Name the blood parasite species.
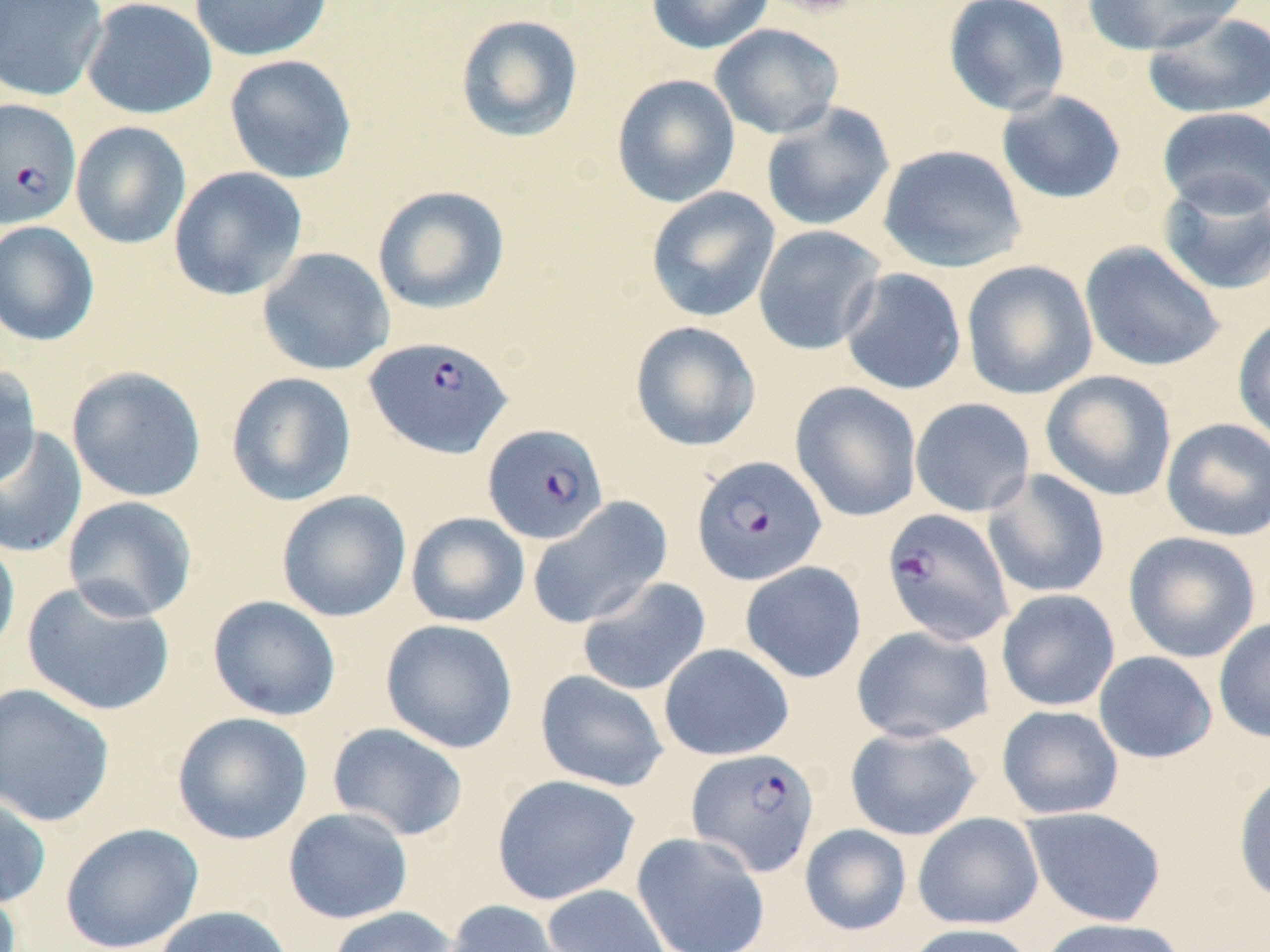
Plasmodium falciparum.

Approximate bounding boxes as (x1, y1, x2, y2) in pixels. Uninfected red blood cell locations: (0, 0, 108, 102), (81, 0, 217, 120), (188, 0, 333, 61), (645, 0, 775, 54), (757, 0, 867, 19), (942, 0, 1070, 116), (1082, 0, 1247, 56), (1141, 11, 1270, 119), (454, 14, 584, 143), (709, 23, 845, 140), (223, 54, 357, 184), (612, 74, 741, 207), (995, 89, 1127, 204), (760, 102, 895, 233), (1156, 107, 1270, 217), (70, 121, 191, 249), (877, 144, 1027, 273), (169, 167, 308, 301), (1157, 177, 1270, 296), (372, 185, 510, 314), (645, 186, 780, 323), (0, 220, 100, 346), (753, 225, 886, 355), (1079, 241, 1225, 373), (256, 247, 395, 376), (961, 260, 1098, 400), (839, 267, 967, 395), (1232, 314, 1270, 447), (630, 320, 762, 452), (0, 364, 41, 489), (66, 366, 206, 502), (1039, 370, 1177, 502), (225, 372, 357, 507), (790, 381, 922, 522), (910, 397, 1035, 517), (1161, 418, 1270, 542), (0, 426, 88, 558), (982, 469, 1110, 599), (276, 490, 412, 623), (527, 495, 672, 630), (62, 496, 198, 622), (405, 512, 530, 628), (0, 530, 20, 667), (1123, 531, 1261, 663), (740, 561, 867, 683), (576, 576, 712, 696), (21, 579, 177, 717), (996, 589, 1120, 711), (207, 595, 341, 721), (1213, 618, 1270, 743), (380, 619, 519, 754), (851, 625, 996, 743), (658, 643, 794, 761), (1093, 651, 1218, 763), (535, 670, 669, 792), (0, 683, 115, 828), (996, 705, 1124, 819), (171, 711, 313, 845), (327, 722, 469, 842), (844, 725, 983, 841), (1233, 769, 1270, 905), (491, 774, 641, 905), (0, 792, 52, 910), (1020, 806, 1167, 927), (283, 807, 414, 924), (913, 813, 1044, 930), (59, 822, 203, 952), (799, 824, 912, 936), (632, 832, 770, 952), (0, 879, 22, 952), (542, 884, 671, 952), (441, 900, 575, 952), (153, 905, 296, 952), (327, 906, 461, 952), (1037, 917, 1186, 952), (903, 922, 1038, 952). Plasmodium falciparum-infected red blood cell locations: (0, 99, 81, 228), (364, 335, 513, 459), (482, 424, 608, 545), (691, 455, 827, 586), (881, 508, 1015, 646), (686, 747, 820, 877). Light microscopy. One field of a larger specimen. Image is 1270×952 pixels. Thin blood film. May-Grünwald-Giemsa-stained preparation. 1000x magnification.